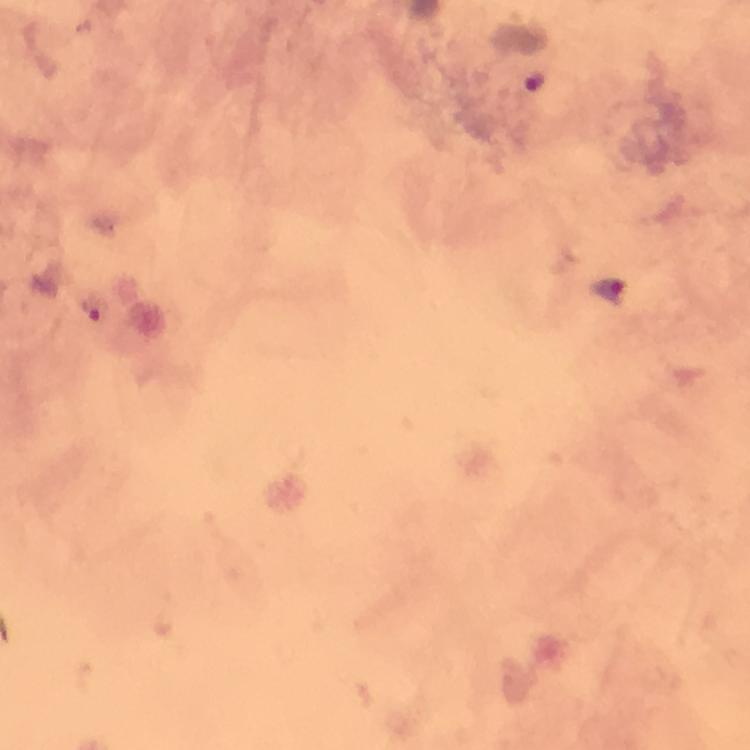
Approximate centers as (x, y) in pixels.
Summary:
  - Malaria parasite locations: (535, 80), (605, 291), (98, 309)
  - Image size: 750×750 pixels
  - Context: from a malaria diagnostic workup
  - Magnification: 100x
  - Preparation: thick smear
  - Cropped from: a single field of view
  - Stain: Giemsa
  - Capture: smartphone mounted on the microscope
  - Immersion oil: used